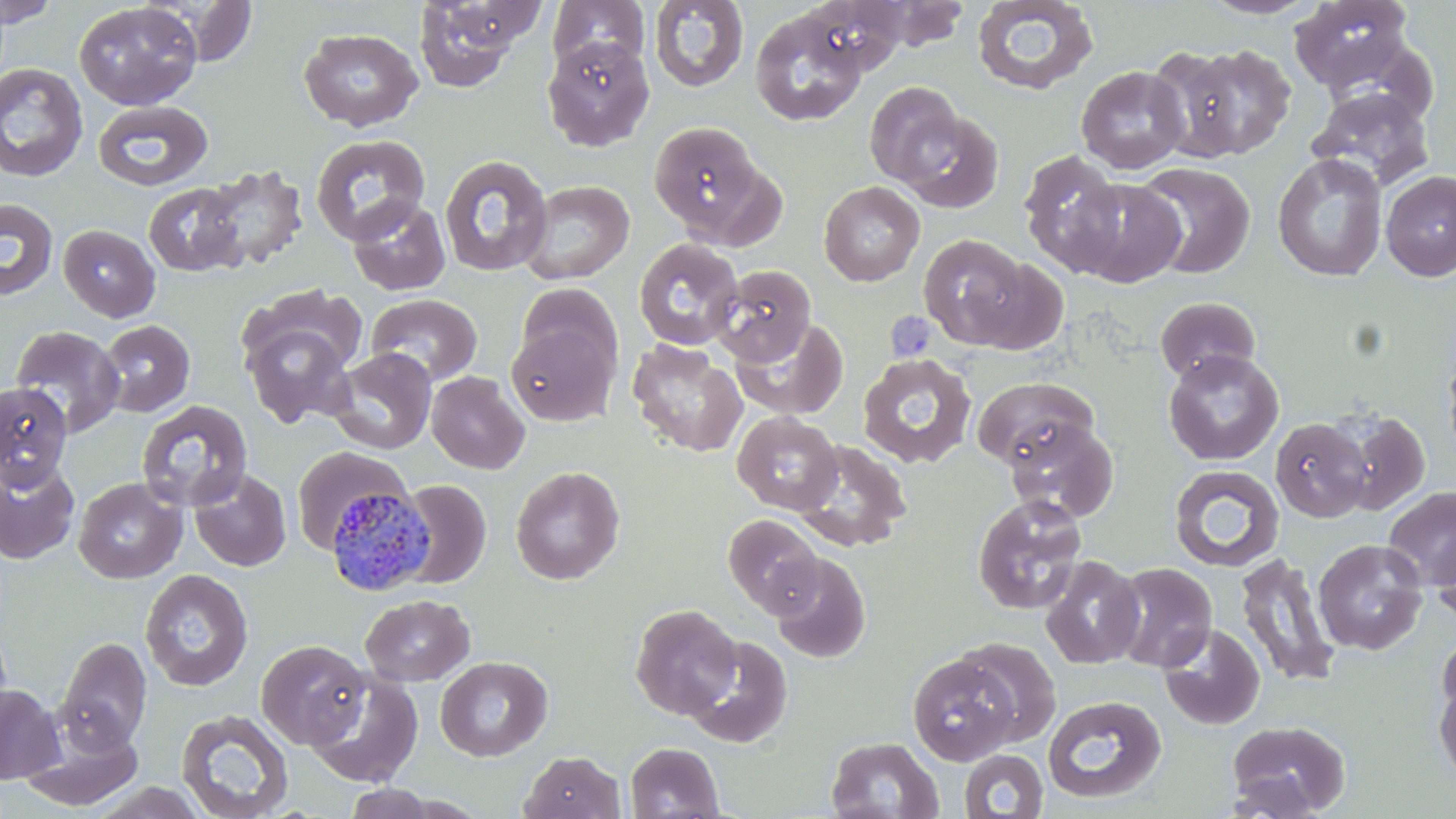

Summary:
  - Coordinate format: approximate bounding boxes as named x1/y1/x2/y2 corners in pixels
  - Uninfected red blood cell locations: (x1=0, y1=0, x2=61, y2=27), (x1=145, y1=0, x2=261, y2=66), (x1=411, y1=0, x2=540, y2=92), (x1=801, y1=0, x2=914, y2=75), (x1=971, y1=0, x2=1099, y2=96), (x1=1199, y1=0, x2=1324, y2=19), (x1=1290, y1=0, x2=1415, y2=93), (x1=547, y1=1, x2=650, y2=76), (x1=648, y1=1, x2=749, y2=93), (x1=847, y1=1, x2=972, y2=51), (x1=73, y1=2, x2=202, y2=110), (x1=749, y1=8, x2=868, y2=126), (x1=298, y1=27, x2=423, y2=131), (x1=541, y1=36, x2=655, y2=151), (x1=1321, y1=36, x2=1440, y2=128), (x1=1163, y1=44, x2=1297, y2=161), (x1=0, y1=63, x2=88, y2=183), (x1=1076, y1=65, x2=1190, y2=174), (x1=864, y1=82, x2=964, y2=186), (x1=1308, y1=87, x2=1434, y2=191), (x1=93, y1=100, x2=213, y2=191), (x1=897, y1=109, x2=1003, y2=212), (x1=649, y1=121, x2=767, y2=240), (x1=309, y1=134, x2=431, y2=244), (x1=1019, y1=150, x2=1127, y2=277), (x1=1272, y1=153, x2=1387, y2=282), (x1=440, y1=154, x2=553, y2=277), (x1=1134, y1=162, x2=1256, y2=280), (x1=198, y1=163, x2=309, y2=272), (x1=1381, y1=170, x2=1456, y2=281), (x1=1065, y1=177, x2=1187, y2=288), (x1=519, y1=180, x2=634, y2=285), (x1=819, y1=181, x2=924, y2=286), (x1=144, y1=182, x2=246, y2=277), (x1=346, y1=197, x2=451, y2=296), (x1=0, y1=198, x2=59, y2=301), (x1=58, y1=224, x2=160, y2=322), (x1=918, y1=234, x2=1034, y2=349), (x1=634, y1=238, x2=744, y2=351), (x1=960, y1=258, x2=1070, y2=356), (x1=711, y1=264, x2=817, y2=366), (x1=517, y1=282, x2=621, y2=376), (x1=240, y1=283, x2=369, y2=377), (x1=366, y1=293, x2=483, y2=386), (x1=1155, y1=296, x2=1261, y2=383), (x1=730, y1=317, x2=848, y2=420), (x1=98, y1=320, x2=196, y2=418), (x1=240, y1=320, x2=357, y2=428), (x1=505, y1=320, x2=619, y2=427), (x1=9, y1=325, x2=126, y2=437), (x1=1441, y1=338, x2=1456, y2=465), (x1=627, y1=339, x2=747, y2=457), (x1=328, y1=347, x2=437, y2=454), (x1=1163, y1=349, x2=1284, y2=466), (x1=856, y1=353, x2=978, y2=468), (x1=426, y1=371, x2=530, y2=474), (x1=972, y1=377, x2=1098, y2=471), (x1=0, y1=383, x2=72, y2=489), (x1=136, y1=400, x2=253, y2=512), (x1=1331, y1=409, x2=1430, y2=516), (x1=732, y1=412, x2=842, y2=514), (x1=1004, y1=416, x2=1118, y2=522), (x1=1271, y1=418, x2=1373, y2=524), (x1=793, y1=439, x2=912, y2=552), (x1=292, y1=445, x2=410, y2=555), (x1=0, y1=456, x2=80, y2=565), (x1=1169, y1=464, x2=1284, y2=572), (x1=510, y1=466, x2=625, y2=585), (x1=188, y1=468, x2=292, y2=573), (x1=73, y1=477, x2=187, y2=584), (x1=397, y1=480, x2=491, y2=588), (x1=1383, y1=487, x2=1456, y2=591), (x1=972, y1=493, x2=1088, y2=615), (x1=723, y1=514, x2=824, y2=617), (x1=1431, y1=527, x2=1456, y2=626), (x1=1313, y1=538, x2=1428, y2=655), (x1=769, y1=552, x2=871, y2=663), (x1=1234, y1=553, x2=1341, y2=688), (x1=1040, y1=555, x2=1146, y2=669), (x1=1109, y1=562, x2=1218, y2=673), (x1=140, y1=569, x2=254, y2=692), (x1=360, y1=594, x2=475, y2=686), (x1=630, y1=604, x2=742, y2=719), (x1=1159, y1=623, x2=1266, y2=730), (x1=1437, y1=629, x2=1456, y2=726), (x1=682, y1=634, x2=793, y2=749), (x1=56, y1=636, x2=152, y2=752), (x1=954, y1=638, x2=1061, y2=746), (x1=256, y1=639, x2=370, y2=749), (x1=907, y1=651, x2=1023, y2=766), (x1=435, y1=656, x2=553, y2=761), (x1=306, y1=671, x2=424, y2=787), (x1=1433, y1=673, x2=1456, y2=786), (x1=0, y1=684, x2=63, y2=784), (x1=1043, y1=695, x2=1166, y2=805), (x1=176, y1=708, x2=295, y2=819), (x1=1225, y1=719, x2=1351, y2=817), (x1=18, y1=721, x2=144, y2=812), (x1=825, y1=736, x2=944, y2=818), (x1=625, y1=742, x2=725, y2=819), (x1=959, y1=749, x2=1049, y2=818), (x1=519, y1=750, x2=625, y2=819), (x1=89, y1=781, x2=210, y2=818), (x1=341, y1=783, x2=442, y2=819)
  - Plasmodium malariae-infected red blood cell locations: (x1=324, y1=483, x2=436, y2=597)
  - Platelet locations: (x1=886, y1=311, x2=936, y2=364)
  - Slide-level diagnosis: Plasmodium malariae
  - Modality: light microscopy
  - Image size: 1456×819 pixels
  - Magnification: 1000x
  - Stain: May-Grünwald-Giemsa
  - Field of view: single
  - Preparation: thin blood film